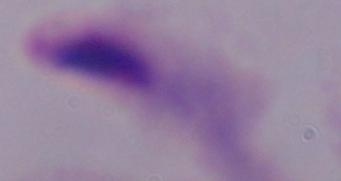

A trichomonad is shown. Photomicrograph. 1000x magnification.